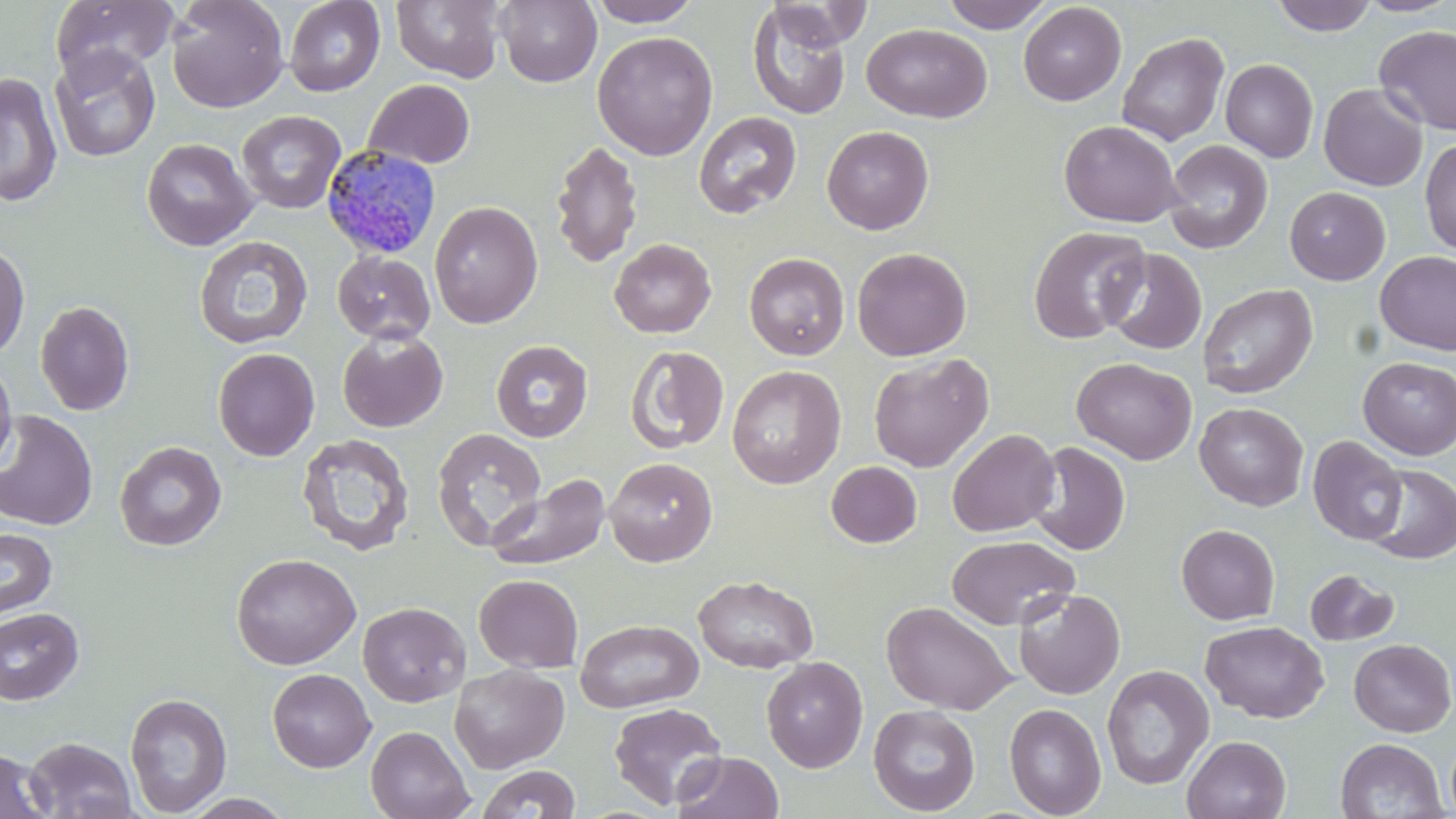
Summary:
  - Coordinate format: approximate bounding boxes as [x1, y1, x2, y2] in pixels
  - Plasmodium malariae-infected red blood cell locations: [321, 144, 442, 259]
  - Uninfected red blood cell locations: [50, 0, 178, 83], [166, 0, 289, 113], [283, 0, 385, 96], [391, 0, 506, 83], [496, 0, 601, 87], [586, 0, 701, 27], [942, 0, 1054, 33], [1271, 0, 1377, 36], [1355, 0, 1456, 17], [765, 1, 871, 50], [1018, 2, 1125, 106], [747, 4, 851, 119], [861, 23, 993, 123], [1374, 25, 1456, 136], [592, 31, 718, 160], [1116, 32, 1229, 147], [49, 45, 161, 162], [1220, 58, 1319, 163], [0, 72, 63, 208], [364, 79, 476, 169], [1318, 83, 1428, 191], [236, 110, 345, 214], [694, 111, 801, 218], [1059, 120, 1183, 227], [822, 125, 934, 234], [141, 138, 258, 251], [1419, 138, 1456, 255], [550, 139, 643, 268], [1163, 140, 1273, 254], [1285, 187, 1390, 285], [428, 201, 543, 328], [1028, 226, 1151, 343], [194, 236, 313, 350], [609, 238, 716, 338], [0, 241, 30, 361], [852, 247, 972, 361], [1101, 248, 1207, 355], [1374, 250, 1456, 355], [332, 251, 436, 344], [744, 252, 850, 360], [1197, 283, 1318, 399], [35, 300, 134, 416], [338, 329, 448, 433], [491, 340, 593, 441], [626, 345, 730, 454], [213, 347, 320, 461], [868, 353, 993, 472], [0, 355, 18, 474], [1072, 357, 1198, 465], [1357, 357, 1456, 460], [727, 364, 846, 489], [1194, 402, 1309, 511], [0, 411, 98, 531], [432, 427, 546, 550], [947, 428, 1061, 537], [297, 433, 415, 557], [1308, 436, 1407, 545], [114, 441, 227, 551], [1029, 441, 1131, 556], [604, 457, 718, 567], [826, 461, 922, 547], [1365, 464, 1456, 564], [486, 474, 611, 571], [1176, 523, 1280, 625], [0, 528, 57, 620], [946, 535, 1079, 630], [231, 553, 361, 669], [1304, 569, 1399, 646], [474, 574, 583, 673], [693, 575, 818, 672], [1013, 588, 1126, 699], [881, 600, 1017, 715], [357, 602, 471, 707], [0, 607, 84, 705], [575, 619, 704, 714], [1201, 621, 1329, 723], [1349, 639, 1455, 737], [761, 656, 868, 773], [450, 664, 569, 773], [1101, 665, 1214, 789], [267, 669, 376, 772], [125, 692, 232, 816], [608, 702, 727, 810], [1004, 703, 1106, 818], [868, 704, 980, 816], [365, 725, 475, 819], [1182, 735, 1291, 819], [1445, 735, 1456, 819], [23, 737, 137, 819], [1335, 738, 1447, 819], [0, 748, 54, 819], [673, 751, 784, 819], [477, 765, 581, 818], [180, 793, 296, 819]
  - Slide-level diagnosis: Plasmodium malariae
  - Stain: May-Grünwald-Giemsa
  - Preparation: thin blood smear
  - Modality: optical microscopy
  - Image size: 1456×819 pixels
  - Field of view: single
  - Magnification: 1000x